State which parasite is depicted.
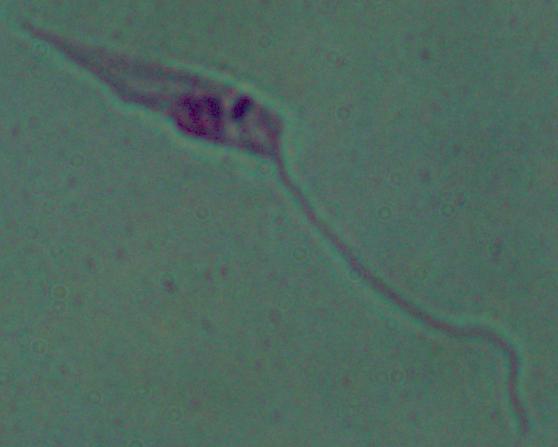

Leishmania.

Summary:
  - Magnification: 1000x
  - Modality: micrograph